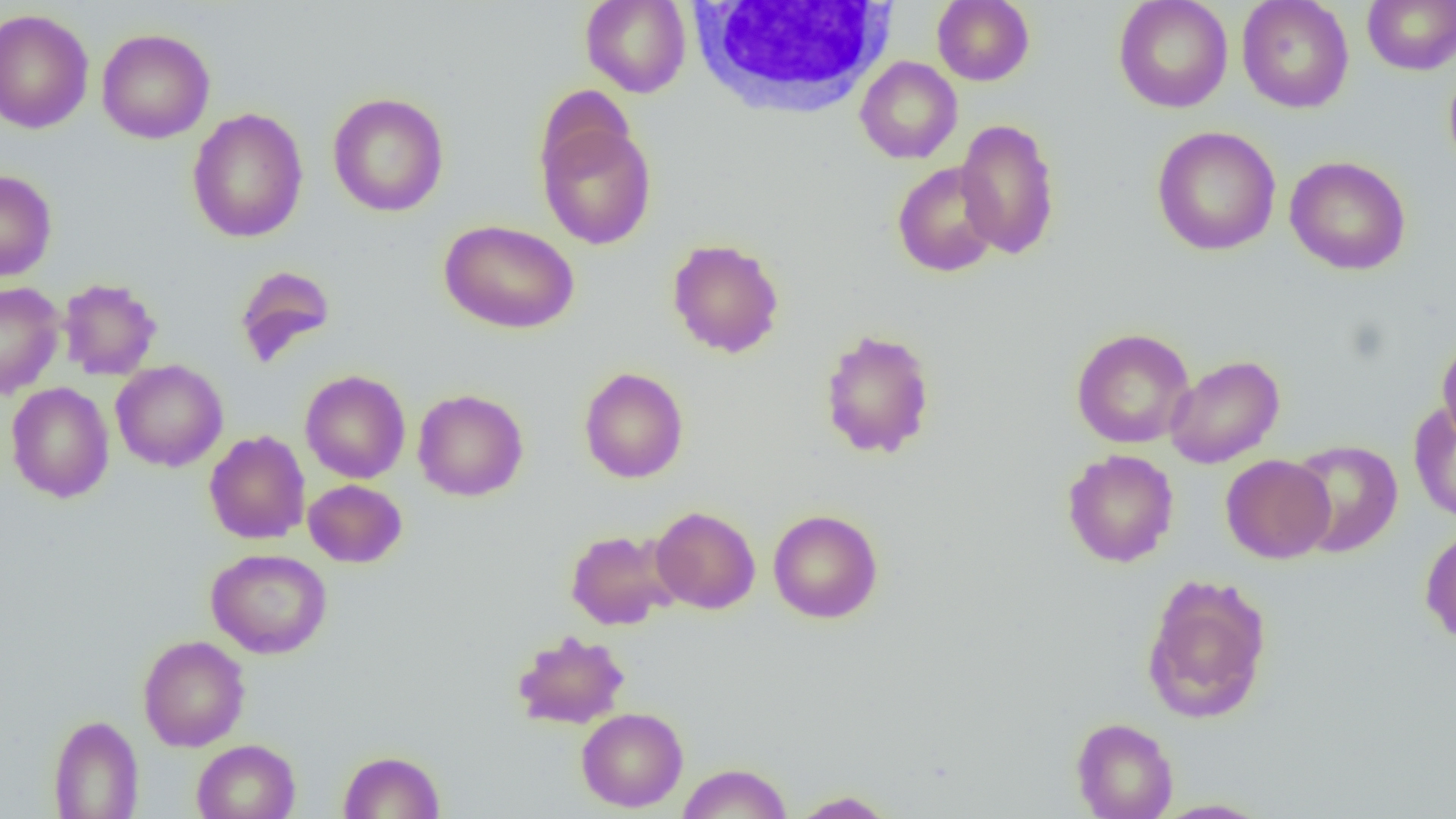

Summary:
  - Coordinate format: approximate bounding boxes as (x1,y1)-(x2,y2) corner pairs in pixels
  - Uninfected red blood cell locations: (580,0)-(691,98), (932,0)-(1034,86), (1113,0)-(1233,113), (1237,0)-(1354,113), (1362,0)-(1456,75), (0,9)-(95,134), (96,28)-(215,143), (855,56)-(962,164), (1444,63)-(1456,180), (327,92)-(450,217), (187,107)-(308,243), (955,118)-(1061,260), (537,119)-(657,250), (1151,125)-(1281,256), (1284,155)-(1411,275), (892,161)-(1002,277), (0,169)-(57,282), (439,219)-(580,335), (667,238)-(784,358), (233,264)-(337,368), (58,277)-(162,380), (0,282)-(65,399), (819,328)-(936,460), (1070,328)-(1195,449), (1437,335)-(1456,450), (1165,354)-(1285,468), (111,360)-(228,472), (578,367)-(689,483), (300,370)-(411,483), (5,382)-(114,503), (413,389)-(528,501), (1408,401)-(1456,524), (204,430)-(310,545), (1288,439)-(1403,557), (1062,448)-(1179,568), (1220,454)-(1335,563), (303,479)-(407,568), (650,506)-(761,614), (768,508)-(884,624), (1420,525)-(1456,646), (564,528)-(681,630), (205,548)-(333,659), (1141,574)-(1273,725), (512,630)-(630,730), (138,635)-(250,752), (576,707)-(688,812), (47,715)-(144,819), (1071,717)-(1178,819), (192,739)-(300,819), (339,750)-(445,818), (676,762)-(793,819), (789,790)-(897,818), (1151,798)-(1272,818)
  - White blood cell locations: (686,1)-(899,120)
  - Slide-level diagnosis: negative for blood parasites
  - Magnification: 1000x
  - Modality: light microscopy
  - Preparation: thin blood smear
  - Image size: 1456×819 pixels
  - Field of view: single